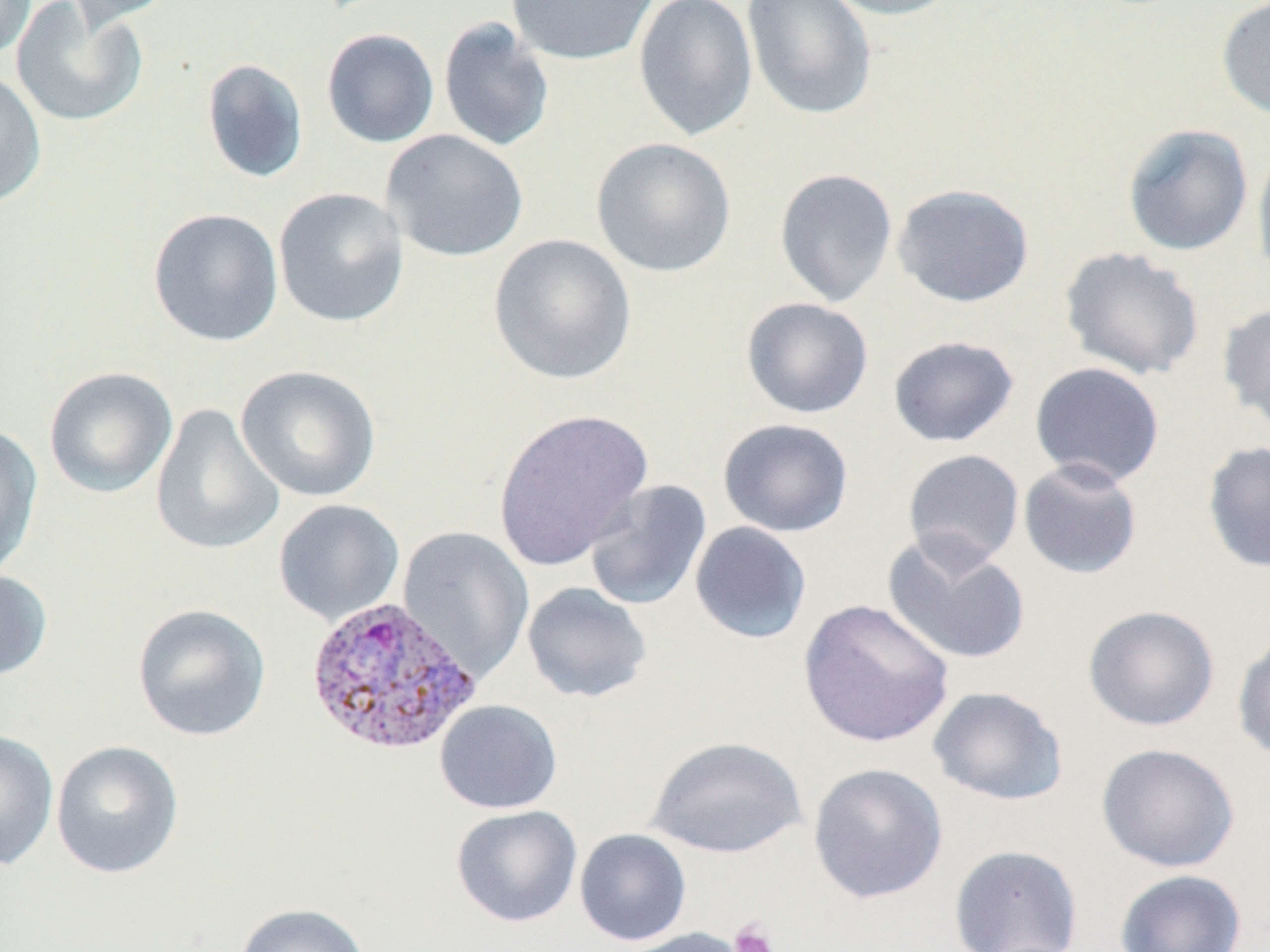 Approximate bounding boxes as named x1/y1/x2/y2 corners in pixels. Platelet locations: (x1=729, y1=919, x2=779, y2=952). Plasmodium vivax-infected red blood cell locations: (x1=303, y1=595, x2=482, y2=757). Uninfected red blood cell locations: (x1=0, y1=0, x2=37, y2=61), (x1=10, y1=0, x2=149, y2=128), (x1=65, y1=0, x2=180, y2=30), (x1=506, y1=0, x2=659, y2=66), (x1=632, y1=0, x2=758, y2=142), (x1=818, y1=0, x2=961, y2=21), (x1=1216, y1=0, x2=1270, y2=121), (x1=741, y1=1, x2=878, y2=122), (x1=438, y1=18, x2=555, y2=153), (x1=321, y1=28, x2=439, y2=148), (x1=201, y1=58, x2=309, y2=184), (x1=0, y1=69, x2=47, y2=209), (x1=1121, y1=123, x2=1254, y2=257), (x1=381, y1=130, x2=529, y2=262), (x1=590, y1=137, x2=737, y2=278), (x1=1252, y1=141, x2=1270, y2=283), (x1=774, y1=168, x2=898, y2=307), (x1=891, y1=182, x2=1035, y2=308), (x1=273, y1=187, x2=409, y2=328), (x1=148, y1=207, x2=284, y2=347), (x1=488, y1=233, x2=637, y2=386), (x1=1059, y1=246, x2=1206, y2=381), (x1=741, y1=296, x2=873, y2=419), (x1=1217, y1=301, x2=1270, y2=433), (x1=888, y1=335, x2=1020, y2=448), (x1=1029, y1=361, x2=1166, y2=488), (x1=235, y1=364, x2=381, y2=502), (x1=43, y1=366, x2=178, y2=499), (x1=151, y1=404, x2=285, y2=556), (x1=492, y1=408, x2=653, y2=571), (x1=717, y1=418, x2=854, y2=537), (x1=0, y1=423, x2=43, y2=580), (x1=1202, y1=440, x2=1270, y2=574), (x1=902, y1=449, x2=1025, y2=570), (x1=1018, y1=458, x2=1144, y2=579), (x1=584, y1=479, x2=712, y2=611), (x1=273, y1=498, x2=405, y2=626), (x1=689, y1=521, x2=812, y2=644), (x1=397, y1=526, x2=534, y2=681), (x1=882, y1=532, x2=1032, y2=667), (x1=0, y1=567, x2=52, y2=681), (x1=521, y1=582, x2=653, y2=704), (x1=797, y1=598, x2=955, y2=748), (x1=131, y1=603, x2=271, y2=742), (x1=1082, y1=604, x2=1220, y2=732), (x1=1232, y1=627, x2=1270, y2=764), (x1=927, y1=686, x2=1068, y2=806), (x1=434, y1=699, x2=563, y2=814), (x1=0, y1=729, x2=59, y2=871), (x1=646, y1=735, x2=808, y2=859), (x1=51, y1=741, x2=184, y2=879), (x1=1096, y1=742, x2=1240, y2=873), (x1=808, y1=763, x2=948, y2=904), (x1=450, y1=805, x2=582, y2=928), (x1=574, y1=829, x2=692, y2=946), (x1=948, y1=844, x2=1084, y2=952), (x1=1114, y1=869, x2=1247, y2=952), (x1=234, y1=902, x2=373, y2=952), (x1=618, y1=927, x2=752, y2=952). Slide-level diagnosis: Plasmodium vivax. Captured at 1000x magnification. Image is 1270×952 pixels. Single field of view. Optical microscopy. Thin blood smear. May-Grünwald-Giemsa-stained preparation.